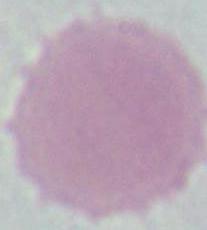

Summary:
  - Identification: erythrocyte
  - Modality: photomicrograph
  - Magnification: 1000x